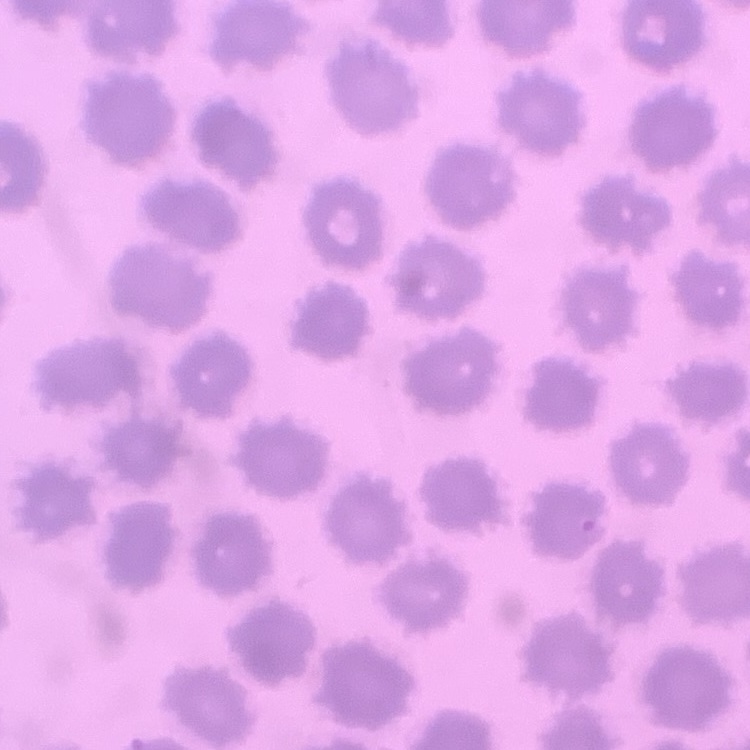 The red blood cells show no rouleaux formation. Field's or Giemsa stain. One tile cut from a larger photomicrograph. Thin blood smear.